Locate every Plasmodium falciparum-infected red blood cell.
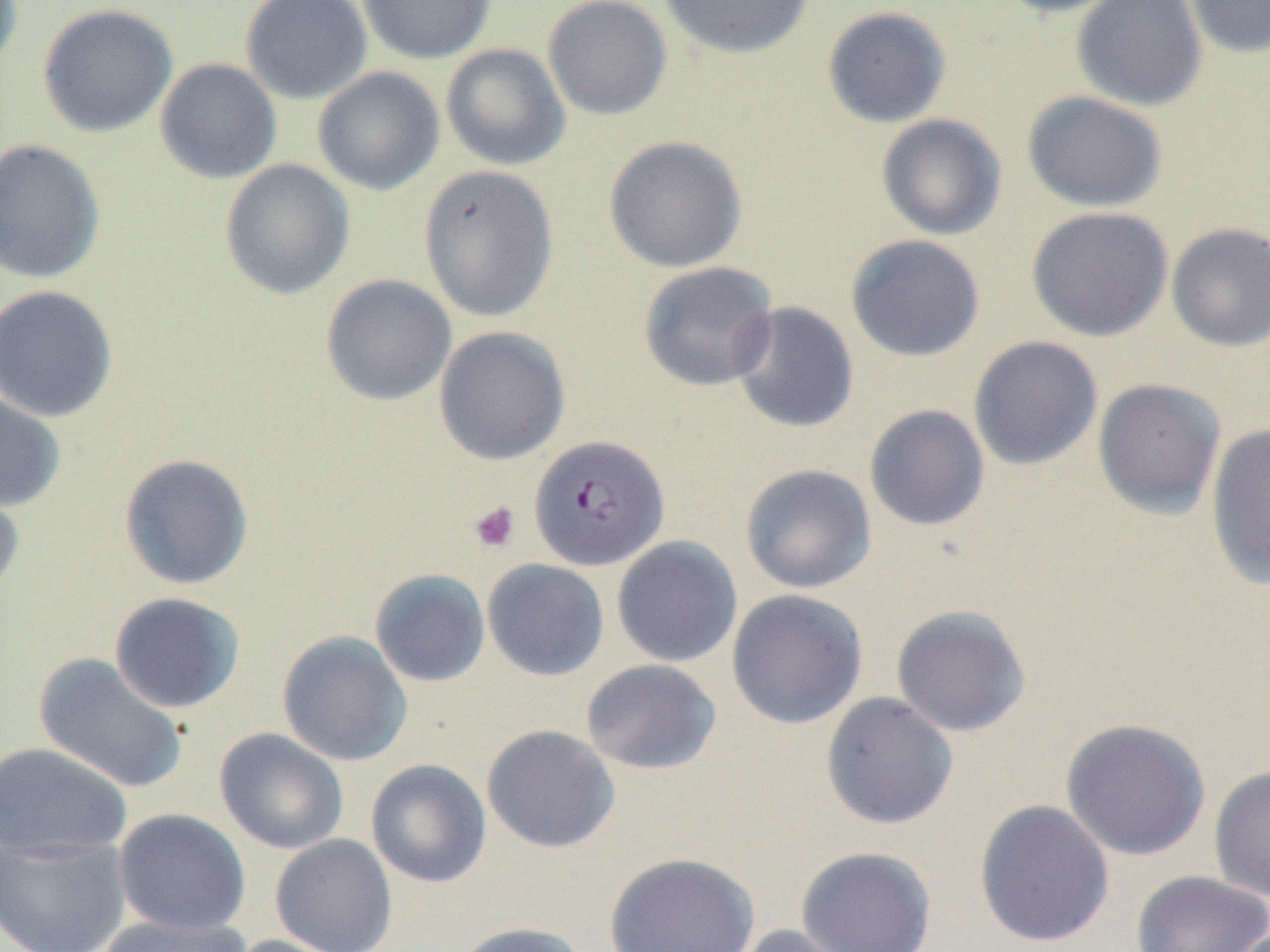
Approximate bounding boxes as [x1, y1, x2, y2] in pixels.
Plasmodium falciparum-infected red blood cells: [529, 434, 670, 571].

Platelet locations: [468, 501, 520, 553]. Uninfected red blood cell locations: [0, 0, 23, 75], [240, 0, 372, 104], [357, 0, 498, 64], [542, 0, 672, 121], [655, 0, 815, 60], [990, 0, 1130, 18], [1071, 0, 1207, 112], [1182, 0, 1270, 58], [37, 3, 177, 137], [822, 5, 952, 128], [440, 43, 570, 171], [155, 58, 282, 184], [312, 66, 445, 195], [1021, 90, 1168, 213], [876, 113, 1007, 240], [603, 135, 747, 272], [0, 138, 106, 284], [219, 159, 355, 300], [417, 164, 560, 322], [1026, 206, 1174, 342], [1165, 221, 1270, 352], [845, 234, 986, 362], [638, 261, 779, 392], [320, 274, 457, 406], [0, 284, 118, 423], [729, 301, 859, 434], [434, 326, 570, 465], [969, 336, 1103, 470], [1092, 378, 1226, 519], [0, 389, 66, 513], [863, 404, 990, 531], [1204, 424, 1270, 589], [118, 453, 254, 590], [740, 463, 877, 594], [0, 477, 25, 599], [611, 536, 742, 667], [482, 559, 610, 681], [369, 568, 491, 687], [726, 589, 868, 729], [109, 591, 246, 714], [890, 604, 1031, 737], [277, 631, 413, 766], [32, 653, 189, 794], [580, 659, 722, 775], [820, 691, 958, 829], [1060, 718, 1211, 861], [481, 724, 621, 853], [214, 728, 349, 855], [0, 741, 133, 861], [366, 758, 492, 888], [1209, 765, 1270, 902], [973, 799, 1115, 948], [113, 808, 251, 936], [0, 834, 131, 952], [270, 834, 397, 952], [795, 846, 937, 952], [604, 851, 760, 952], [1130, 870, 1270, 952], [98, 913, 251, 952], [450, 921, 589, 952], [732, 924, 858, 952], [222, 933, 357, 952]. Slide-level diagnosis: Plasmodium falciparum. Image is 1270×952 pixels. Optical microscopy. Single field of view. Thin blood film. 1000x magnification. May-Grünwald-Giemsa-stained preparation.